Identify the parasite.
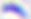

Toxoplasma gondii.

Summary:
  - Magnification: 400x
  - Modality: micrograph